Report the malaria status of this cell.
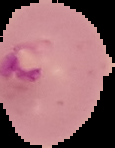
Parasitized.

Summary:
  - Image type: segmented cell region on a black background
  - Preparation: thin blood film
  - Image size: 115×148 pixels